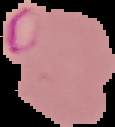
The area outside the segmented cell region is set to black. From a thin blood film. Image is 115×127 pixels. Result: malaria parasites detected.